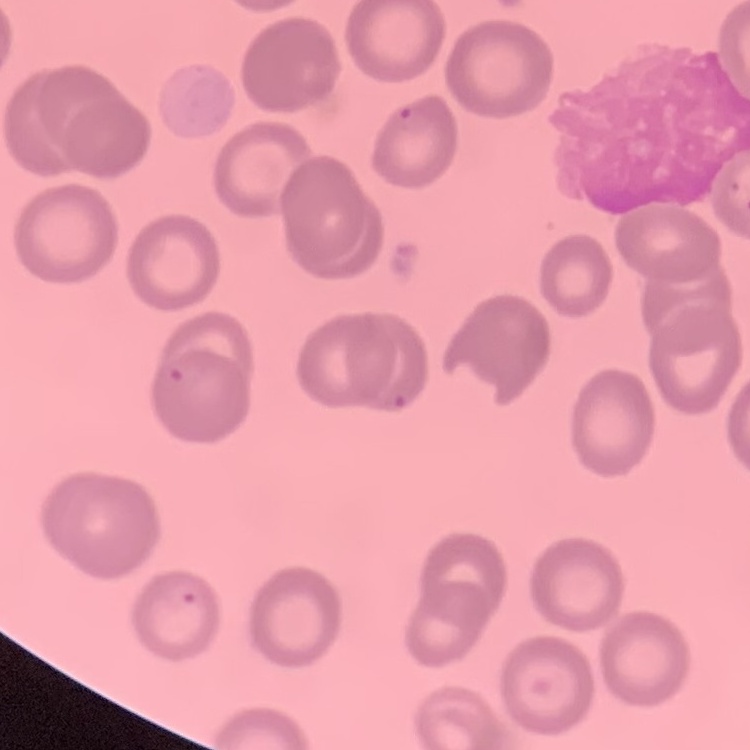
Summary:
  - Erythrocyte morphology: no rouleaux formation
  - Preparation: thin blood film
  - Image type: square crop of a larger photomicrograph
  - Stain: Field's or Giemsa